Locate every blood parasite and identify its species.
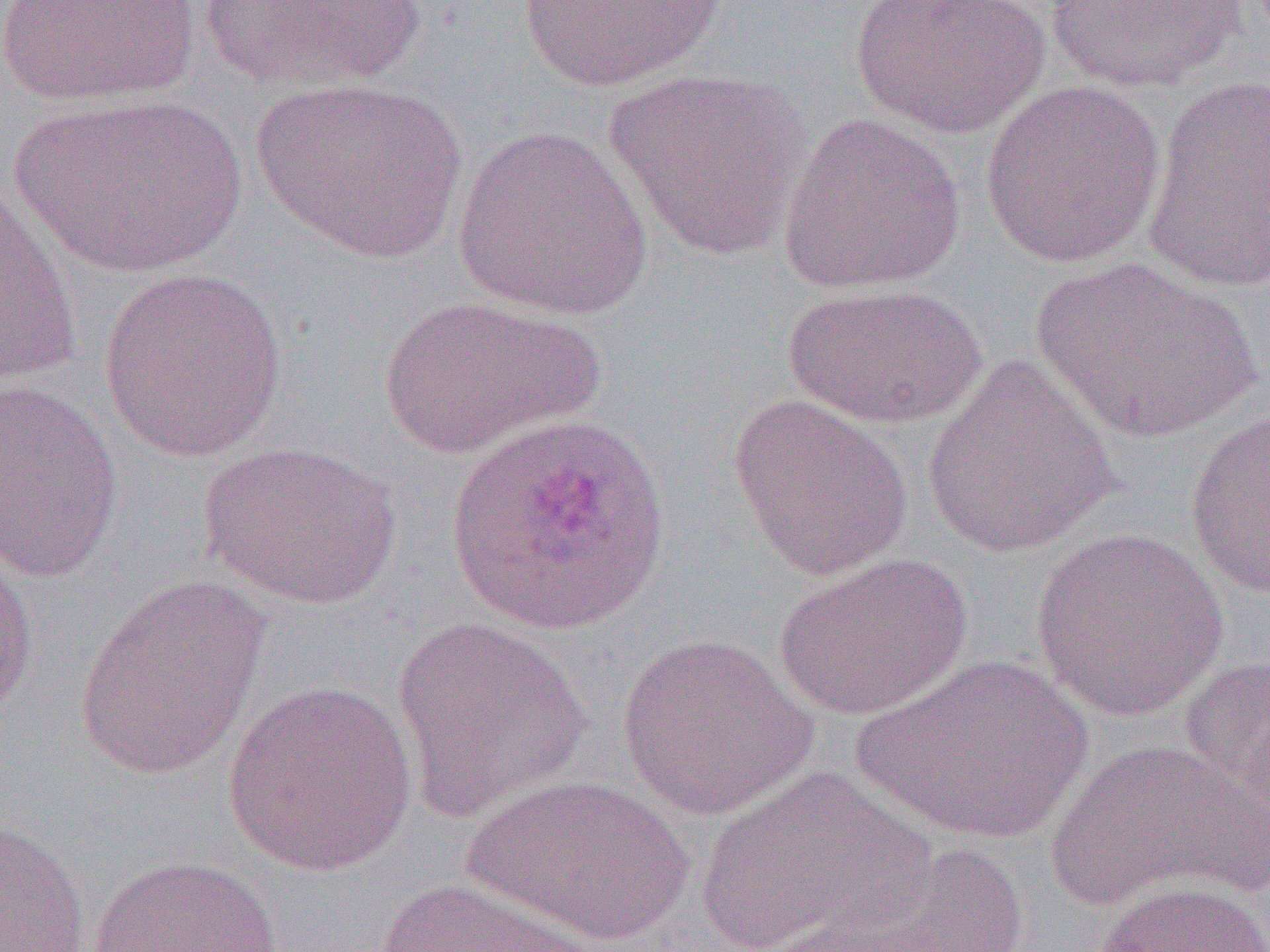
Approximate bounding boxes as [x1, y1, x2, y2] in pixels.
Plasmodium ovale-infected red blood cells: [445, 411, 670, 637].
No Plasmodium falciparum, Plasmodium malariae, Plasmodium vivax, Babesia divergens, or Trypanosoma brucei observed.

slide-level diagnosis = Plasmodium ovale
preparation = thin blood smear
uninfected red blood cell locations = approximate bounding boxes as [x1, y1, x2, y2] in pixels: [0, 0, 201, 108], [201, 0, 424, 94], [517, 0, 726, 92], [848, 0, 1051, 139], [1044, 0, 1247, 93], [601, 69, 815, 262], [1142, 74, 1270, 294], [250, 77, 468, 263], [978, 78, 1166, 269], [13, 93, 246, 279], [776, 111, 967, 295], [453, 124, 653, 321], [1, 182, 84, 387], [1030, 257, 1261, 445], [98, 266, 290, 461], [783, 283, 987, 429], [374, 295, 602, 460], [921, 355, 1122, 558], [0, 378, 124, 584], [728, 394, 913, 580], [1184, 406, 1270, 599], [198, 441, 402, 610], [1030, 529, 1230, 722], [0, 547, 40, 723], [773, 552, 972, 721], [73, 574, 271, 782], [392, 617, 591, 822], [616, 631, 819, 821], [854, 653, 1094, 847], [1177, 653, 1270, 828], [222, 679, 419, 876], [1043, 738, 1269, 914], [694, 765, 935, 951], [462, 773, 694, 947], [1, 814, 91, 952], [852, 843, 1031, 952], [84, 854, 286, 952], [370, 877, 605, 952], [1093, 879, 1269, 952], [743, 889, 989, 952]
modality = optical microscopy
magnification = 1000x
field of view = single
image size = 1270×952 pixels